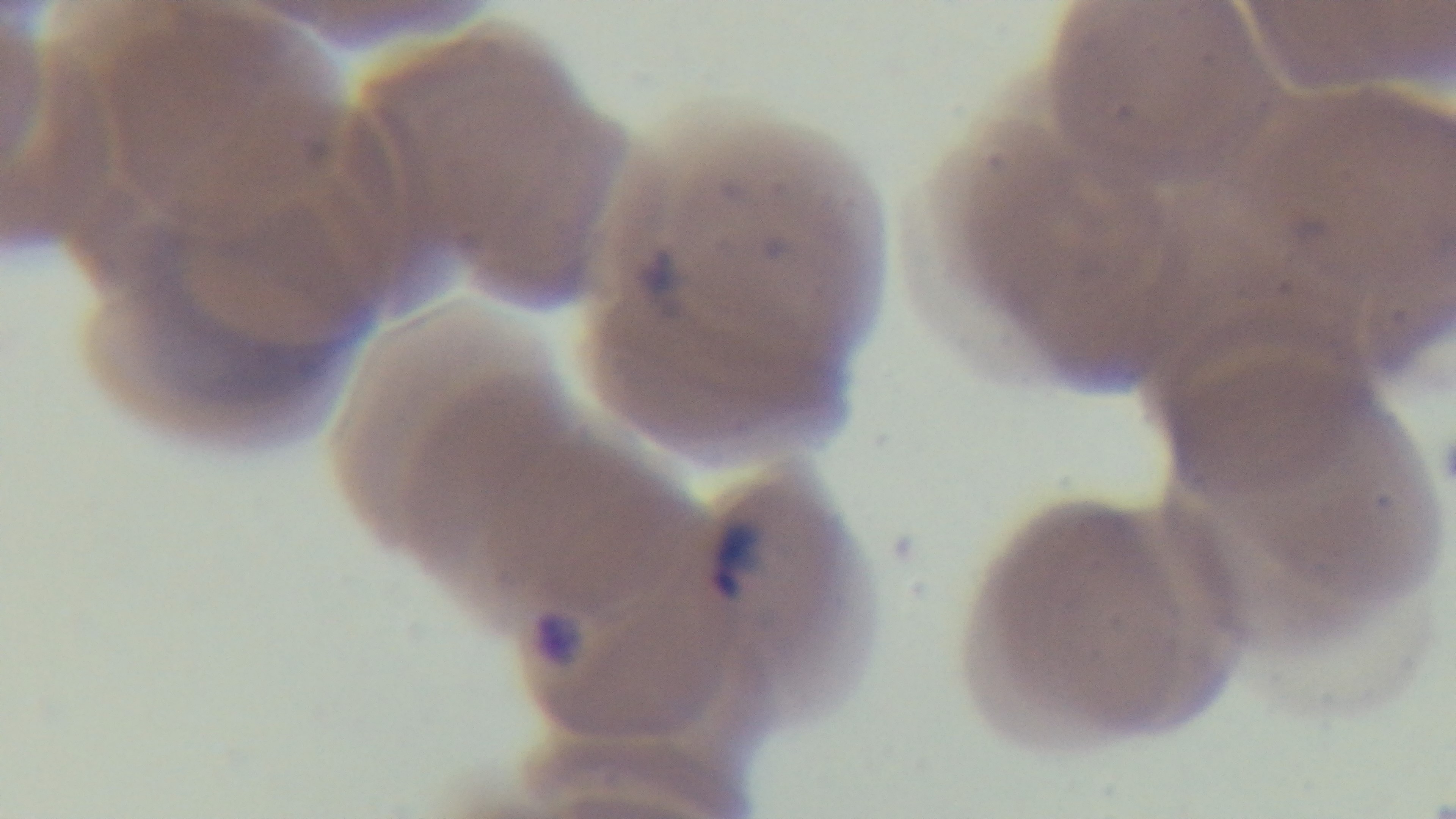 Preparation: thin. Photomicrograph. Single field of view. Captured with a mounted 4K digital camera. Giemsa-stained. 100x oil-immersion objective. Malaria status: positive.